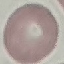

Summary:
  - Result: no malaria parasites seen
  - Capture: smartphone through the microscope eyepiece
  - Image type: cell patch, automatically extracted from a larger field of view and resized to 64 × 64 pixels
  - Preparation: thin blood film
  - Stain: Giemsa